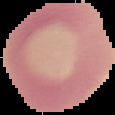
Summary:
  - Image type: segmented cell region on a black background
  - Preparation: thin blood smear
  - Image size: 115×115 pixels
  - Malaria status: uninfected